Assess the morphology of the erythrocytes.
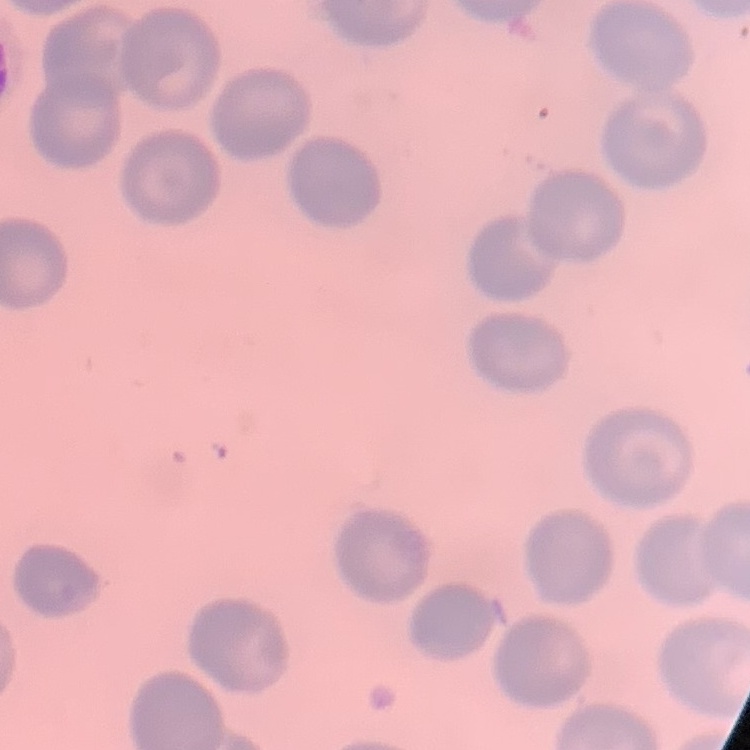

They show no rouleaux formation.

Summary:
  - Stain: Field's or Giemsa
  - Preparation: thin blood film
  - Image type: one tile cut from a larger photomicrograph